Outline each blood parasite and name the species.
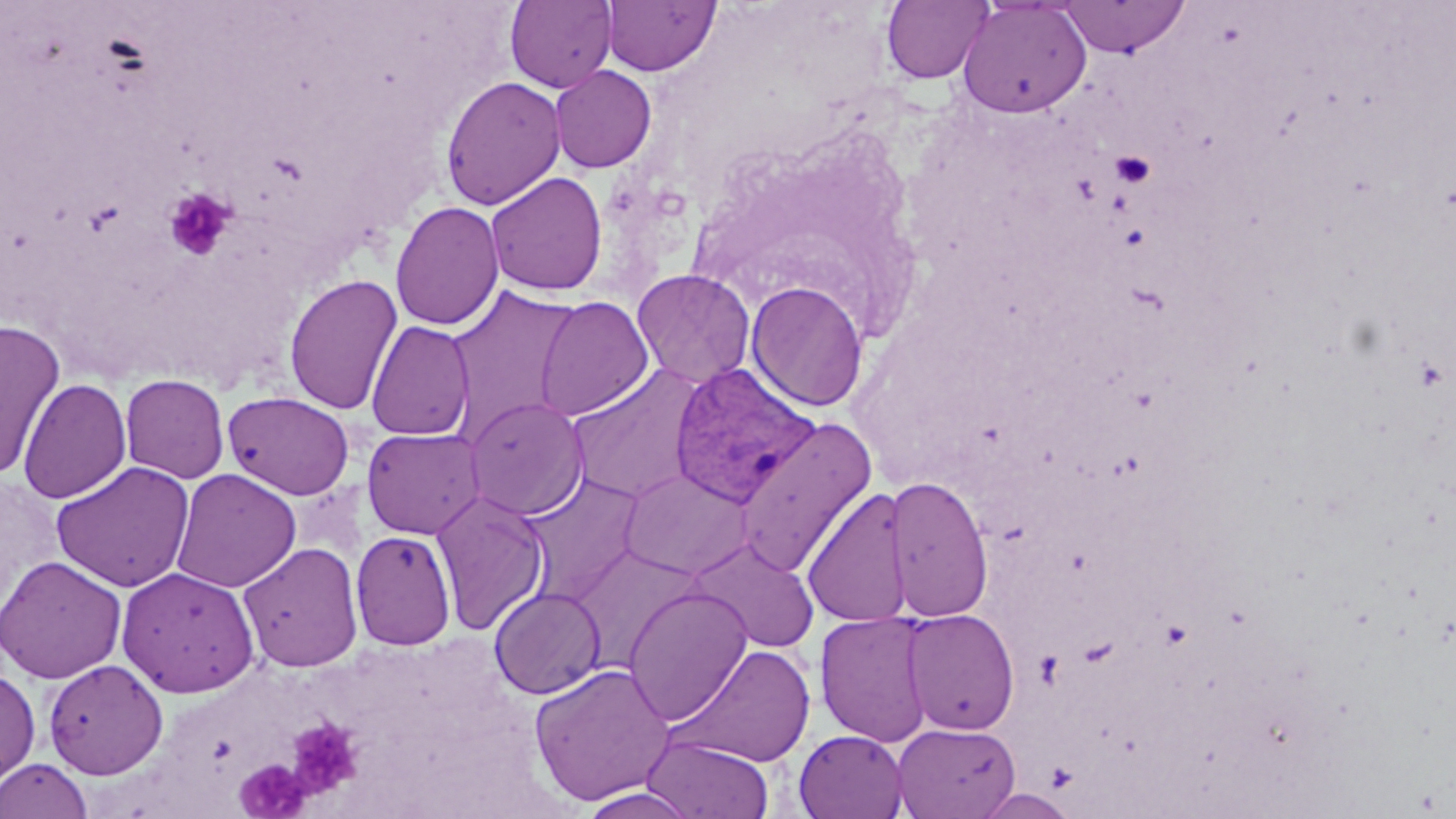

Approximate bounding boxes as named x1/y1/x2/y2 corners in pixels.
Plasmodium vivax-infected red blood cells: (x1=669, y1=362, x2=821, y2=508).
No Plasmodium falciparum, Plasmodium ovale, Plasmodium malariae, Babesia divergens, or Trypanosoma brucei observed.

Uninfected red blood cell locations: (x1=505, y1=0, x2=616, y2=92), (x1=602, y1=0, x2=720, y2=76), (x1=881, y1=0, x2=992, y2=84), (x1=958, y1=0, x2=1092, y2=118), (x1=1059, y1=0, x2=1190, y2=58), (x1=550, y1=65, x2=657, y2=173), (x1=440, y1=75, x2=566, y2=210), (x1=485, y1=171, x2=608, y2=296), (x1=390, y1=200, x2=504, y2=331), (x1=631, y1=269, x2=756, y2=389), (x1=284, y1=272, x2=403, y2=416), (x1=745, y1=280, x2=869, y2=412), (x1=444, y1=284, x2=581, y2=433), (x1=534, y1=296, x2=654, y2=421), (x1=0, y1=319, x2=66, y2=479), (x1=366, y1=320, x2=475, y2=441), (x1=566, y1=363, x2=706, y2=505), (x1=119, y1=373, x2=230, y2=484), (x1=17, y1=378, x2=131, y2=504), (x1=222, y1=390, x2=355, y2=499), (x1=463, y1=396, x2=589, y2=519), (x1=733, y1=416, x2=877, y2=578), (x1=362, y1=427, x2=486, y2=540), (x1=50, y1=461, x2=196, y2=592), (x1=171, y1=468, x2=301, y2=592), (x1=618, y1=469, x2=755, y2=580), (x1=519, y1=473, x2=645, y2=604), (x1=887, y1=475, x2=993, y2=621), (x1=802, y1=486, x2=912, y2=628), (x1=431, y1=490, x2=550, y2=637), (x1=350, y1=529, x2=456, y2=651), (x1=687, y1=536, x2=820, y2=653), (x1=239, y1=542, x2=363, y2=673), (x1=567, y1=546, x2=706, y2=671), (x1=0, y1=554, x2=127, y2=684), (x1=116, y1=566, x2=260, y2=697), (x1=489, y1=586, x2=606, y2=699), (x1=623, y1=586, x2=754, y2=726), (x1=901, y1=608, x2=1020, y2=735), (x1=815, y1=612, x2=936, y2=746), (x1=670, y1=644, x2=816, y2=766), (x1=42, y1=659, x2=168, y2=779), (x1=529, y1=663, x2=675, y2=805), (x1=0, y1=664, x2=40, y2=790), (x1=893, y1=722, x2=1020, y2=819), (x1=793, y1=729, x2=908, y2=818), (x1=642, y1=735, x2=775, y2=819), (x1=1, y1=758, x2=93, y2=819), (x1=577, y1=788, x2=702, y2=819), (x1=975, y1=789, x2=1080, y2=818). Platelet locations: (x1=1110, y1=150, x2=1156, y2=187), (x1=163, y1=186, x2=236, y2=262), (x1=285, y1=717, x2=364, y2=800), (x1=236, y1=759, x2=309, y2=817). Slide-level diagnosis: Plasmodium vivax. Image is 1456×819 pixels. May-Grünwald-Giemsa-stained preparation. Thin blood smear. Single field of view. Captured at 1000x magnification. Light microscopy.